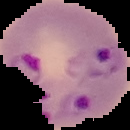 Image is 130×130 pixels. From a thin blood smear. Result: malaria parasites identified. Segmented cell region on a black background.